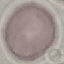

Summary:
  - Result: no malaria parasites seen
  - Preparation: thin smear
  - Capture: smartphone camera at the microscope eyepiece
  - Stain: Giemsa
  - Image type: automatically extracted cell patch, resized to 64 × 64 pixels